Assess the morphology of the red blood cells.
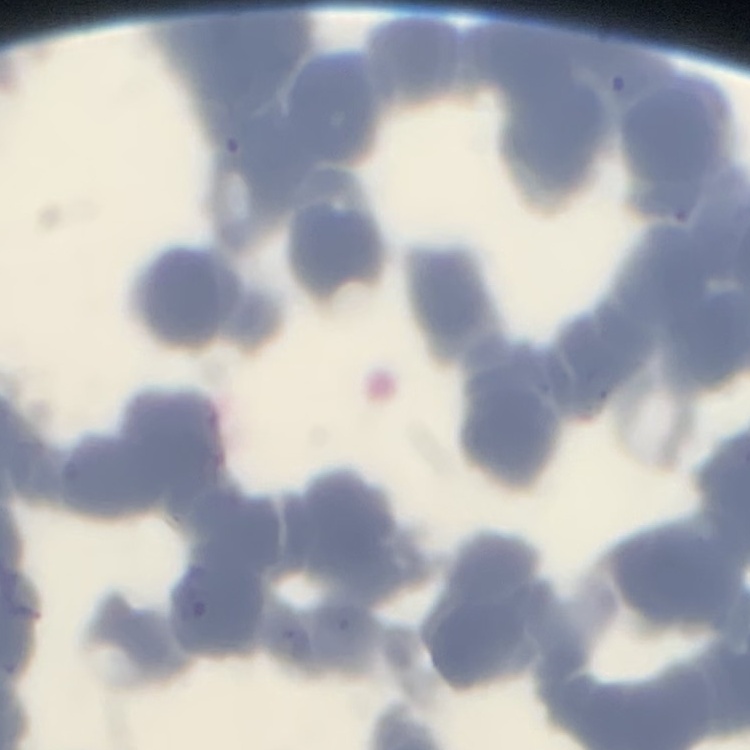
They show rouleaux formation.

Summary:
  - Image type: square crop of a larger photomicrograph
  - Stain: Field's or Giemsa
  - Preparation: thin blood film